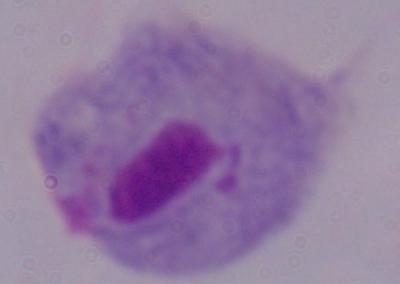
Summary:
  - Modality: micrograph
  - Magnification: 1000x
  - Identification: trichomonad